Report the malaria status of this cell.
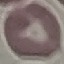

Uninfected.

Photographed with a smartphone camera at the microscope eyepiece. Thin blood smear. Cell patch, automatically extracted from a larger field of view and resized to 64 × 64 pixels. Giemsa-stained preparation.